Report the malaria status of this cell.
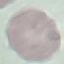
It is uninfected.

Giemsa stain. Photographed with a smartphone camera at the microscope eyepiece. Thin blood smear. Automatically extracted cell patch, resized to 64 × 64 pixels.